Name the parasite shown.
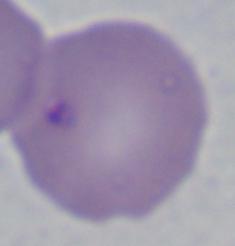

Babesia.

modality = micrograph
magnification = 1000x